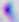

{
  "modality": "micrograph",
  "identification": "Toxoplasma gondii",
  "magnification": "400x"
}